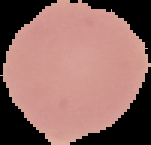
Cell region segmented out of the field of view; the surrounding area is masked to black. From a thin blood film. Result: no malaria parasites detected. Image is 151×145 pixels.